Locate and identify every blood parasite.
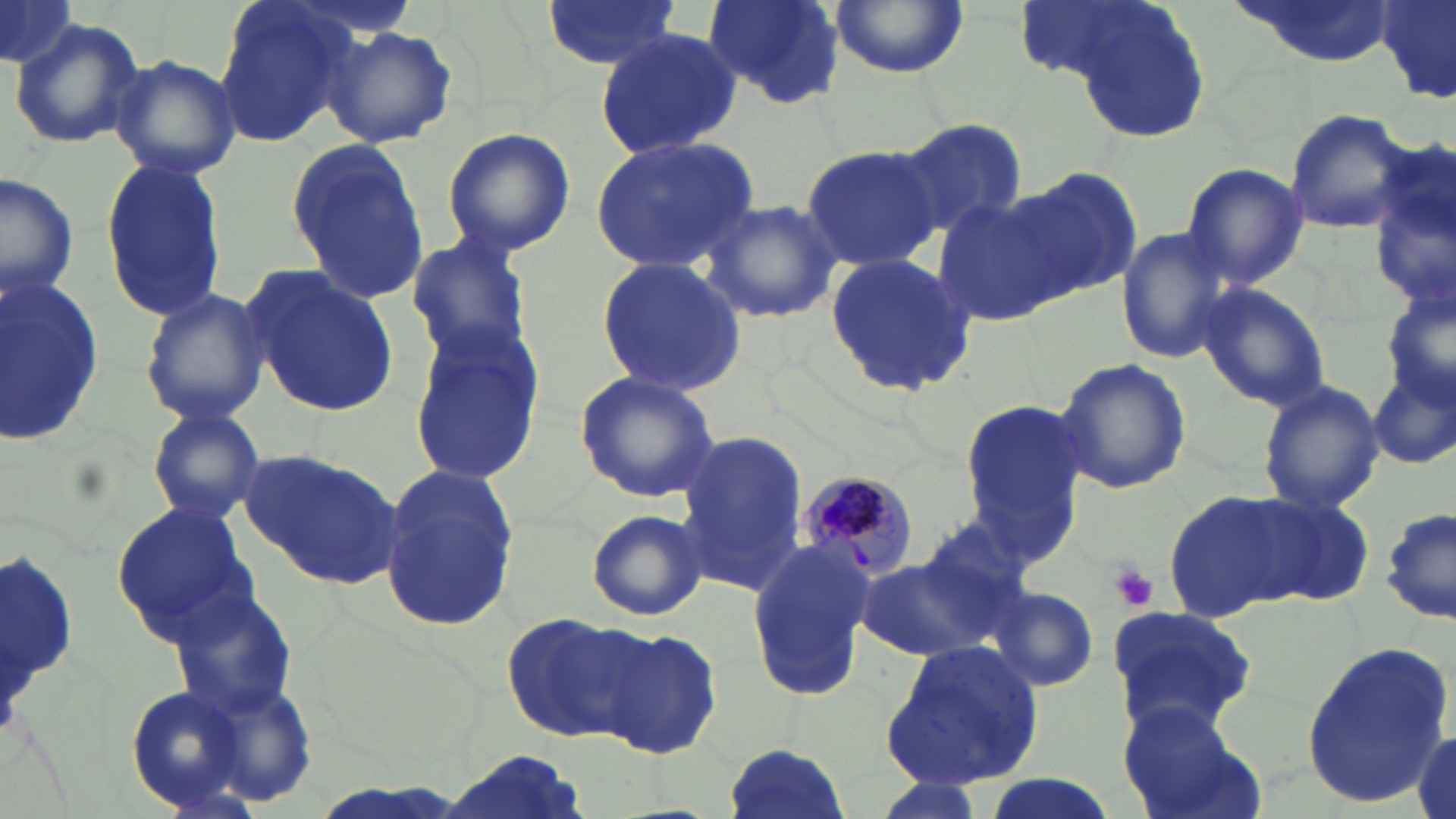
Approximate bounding boxes as [x1, y1, x2, y2] in pixels.
Plasmodium malariae-infected red blood cells: [798, 468, 922, 582].
No Plasmodium falciparum, Plasmodium ovale, Plasmodium vivax, Babesia divergens, or Trypanosoma brucei observed.

Summary:
  - Uninfected red blood cell locations: [0, 0, 79, 72], [212, 0, 364, 150], [698, 0, 848, 110], [828, 0, 970, 78], [1235, 0, 1394, 67], [539, 1, 683, 72], [1052, 2, 1213, 147], [1376, 2, 1456, 106], [9, 19, 145, 151], [321, 23, 457, 148], [594, 27, 740, 161], [109, 54, 240, 181], [1282, 108, 1413, 234], [895, 117, 1027, 238], [440, 126, 578, 260], [285, 134, 434, 307], [591, 135, 760, 274], [800, 142, 940, 273], [1369, 142, 1455, 320], [99, 155, 226, 323], [1178, 163, 1310, 289], [1012, 164, 1145, 302], [0, 172, 79, 303], [932, 192, 1072, 326], [701, 196, 842, 324], [1115, 226, 1240, 365], [405, 232, 536, 367], [822, 253, 981, 399], [595, 257, 748, 396], [242, 263, 403, 417], [0, 275, 106, 448], [1197, 281, 1332, 412], [139, 285, 269, 426], [405, 320, 547, 484], [1054, 355, 1191, 495], [1371, 366, 1454, 474], [574, 370, 721, 504], [1256, 379, 1386, 513], [957, 398, 1092, 543], [143, 401, 266, 525], [675, 431, 810, 593], [238, 448, 407, 589], [377, 463, 519, 631], [1163, 489, 1299, 621], [1255, 494, 1377, 607], [112, 499, 253, 641], [1379, 507, 1455, 622], [586, 509, 706, 622], [913, 515, 1040, 631], [748, 534, 875, 702], [855, 555, 1008, 664], [164, 584, 299, 720], [988, 586, 1100, 693], [1105, 605, 1259, 738], [499, 612, 648, 743], [594, 628, 725, 760], [1301, 639, 1452, 805], [881, 641, 1046, 791], [203, 680, 318, 808], [124, 683, 250, 812], [1118, 699, 1262, 819], [1409, 728, 1455, 819], [720, 740, 851, 819], [432, 752, 593, 819], [970, 774, 1123, 819]
  - White blood cell locations: [1, 538, 83, 752]
  - Platelet locations: [1109, 566, 1158, 612]
  - Slide-level diagnosis: Plasmodium malariae
  - Image size: 1456×819 pixels
  - Modality: light microscopy
  - Field of view: single
  - Magnification: 1000x
  - Stain: May-Grünwald-Giemsa
  - Preparation: thin blood film